Assess this cell for malaria.
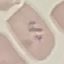
Parasitized.

Automatically extracted cell patch, resized to 64 × 64 pixels. Photographed with a smartphone camera at the microscope eyepiece. Thin blood film. Giemsa stain.